Assess this cell for malaria.
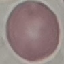
It is uninfected.

Giemsa stain. Thin smear of blood. Acquired by smartphone through the microscope eyepiece. Automatically extracted cell patch, resized to 64 × 64 pixels.